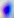 Toxoplasma gondii is shown. Captured at 400x magnification. Micrograph.